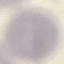

{
  "malaria_status": "uninfected",
  "capture": "smartphone camera at the microscope eyepiece",
  "preparation": "thin smear",
  "image_type": "cell patch, automatically extracted from a larger field of view and resized to 64 × 64 pixels",
  "stain": "Giemsa"
}